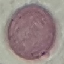

result: no malaria parasites detected
stain: Giemsa
image_type: automatically extracted cell patch, resized to 64 × 64 pixels
capture: smartphone through the microscope eyepiece
preparation: thin blood smear